Report the malaria status of this cell.
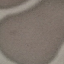
Uninfected.

{
  "preparation": "thin blood smear",
  "capture": "smartphone camera at the microscope eyepiece",
  "image_type": "automatically extracted cell patch, resized to 64 × 64 pixels",
  "stain": "Giemsa"
}